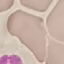 Malaria status: uninfected. Photographed with a smartphone camera at the microscope eyepiece. Cell patch, automatically extracted from a larger field of view and resized to 64 × 64 pixels. Giemsa stain. Thin blood smear.